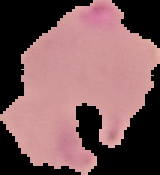 Image is 160×175 pixels. Result: Plasmodium parasites detected. Segmented cell region on a black background. From a thin blood film.